Locate every Plasmodium parasite and every leukocyte.
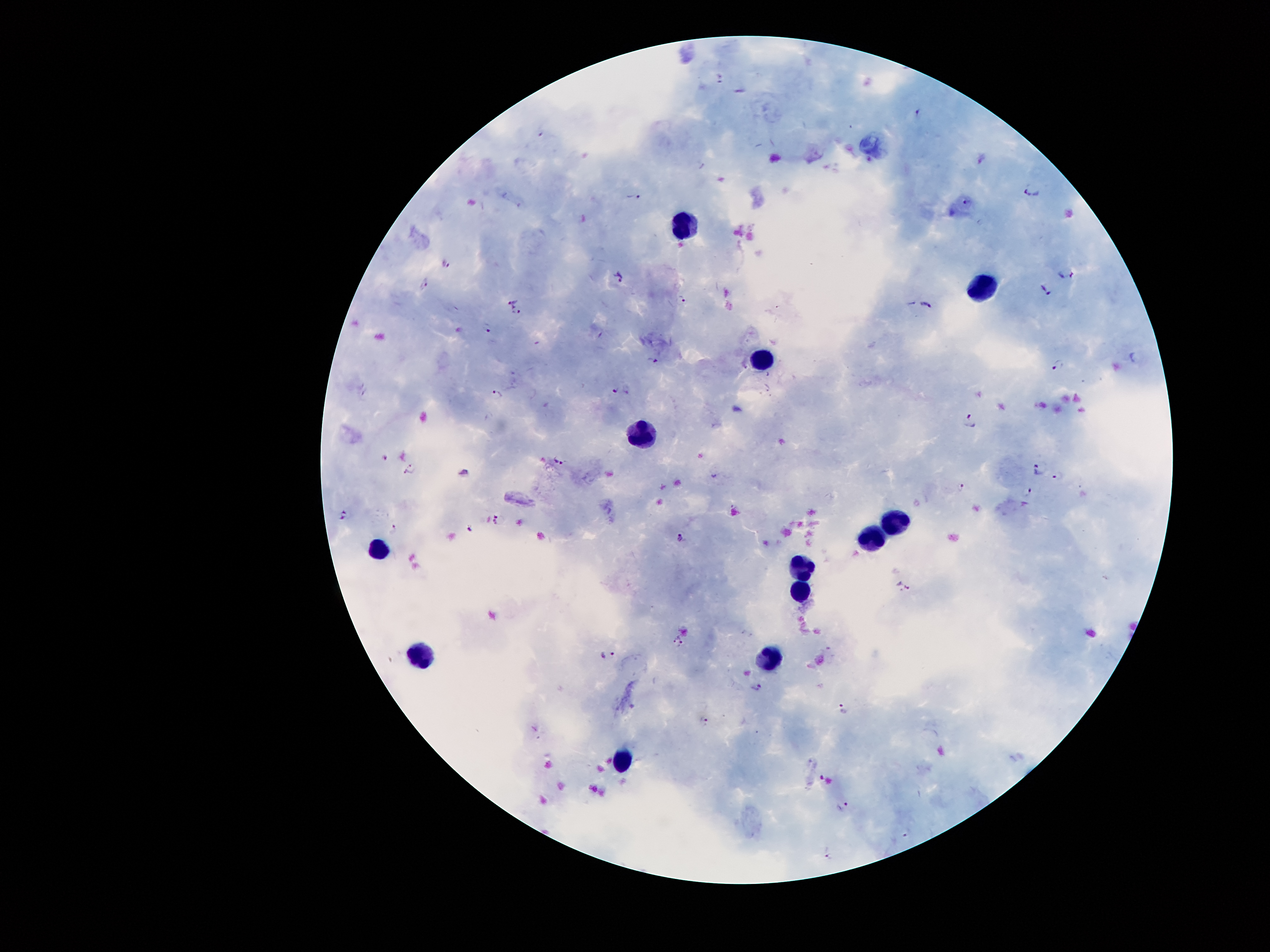

Approximate centers as (x, y) in pixels.
Plasmodium parasites: (720, 77), (917, 112), (1032, 190), (634, 198), (967, 205), (446, 264), (1066, 275), (621, 276), (426, 283), (1045, 291), (683, 300), (512, 302), (927, 304), (518, 313), (487, 329), (653, 362), (1058, 363), (615, 387), (627, 390), (495, 395), (971, 420), (385, 456), (559, 462), (411, 466), (1038, 469), (463, 471), (1058, 476), (961, 486), (1027, 493), (341, 514), (497, 521), (395, 529), (470, 530), (680, 537), (903, 586), (677, 641), (608, 655), (758, 687), (844, 708), (704, 719), (842, 806), (907, 833), (829, 854).
Leukocytes: (678, 223), (979, 285), (763, 359), (640, 437), (897, 522), (871, 544), (380, 546), (802, 566), (804, 588), (774, 654), (422, 658), (619, 753).

Image is 1270×952 pixels. Single field of view. Patient malaria status: positive for Plasmodium falciparum. Giemsa stain. 100x magnification. Smartphone photograph taken through the microscope eyepiece. Thick blood film.